Report the malaria status of this cell.
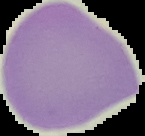

It is uninfected.

{
  "preparation": "thin blood smear",
  "image_size": "145×136 pixels",
  "image_type": "segmented cell region on a black background"
}